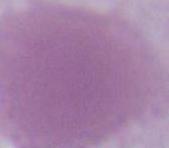

magnification = 1000x
identification = erythrocyte
modality = photomicrograph